State the blood parasite species.
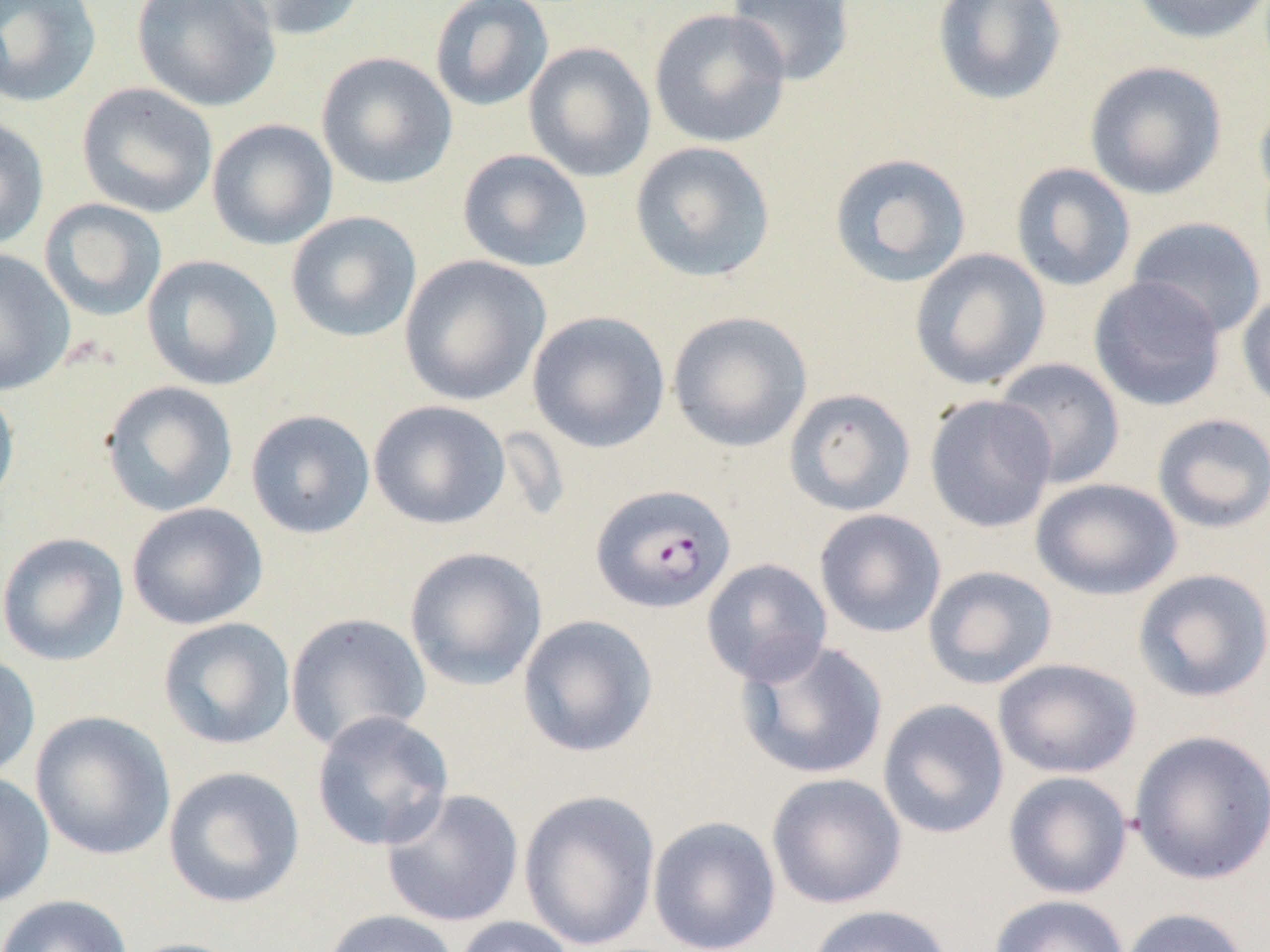

Plasmodium falciparum.

Approximate bounding boxes as (x1, y1, x2, y2) in pixels. Plasmodium falciparum-infected red blood cell locations: (590, 482, 736, 614). Uninfected red blood cell locations: (0, 0, 103, 108), (130, 0, 281, 112), (221, 0, 367, 41), (429, 0, 554, 112), (724, 0, 856, 86), (931, 0, 1068, 107), (1132, 0, 1270, 44), (648, 7, 792, 149), (523, 41, 657, 183), (316, 51, 458, 190), (1084, 61, 1227, 200), (76, 81, 219, 218), (1254, 91, 1270, 212), (0, 116, 50, 251), (206, 118, 338, 251), (629, 141, 777, 283), (456, 149, 593, 273), (827, 152, 972, 288), (1010, 162, 1136, 292), (39, 198, 167, 322), (285, 211, 422, 343), (1127, 216, 1267, 339), (0, 248, 76, 396), (909, 248, 1051, 391), (141, 254, 283, 391), (398, 255, 551, 406), (1088, 275, 1227, 411), (1236, 288, 1270, 414), (667, 310, 813, 453), (527, 311, 671, 453), (992, 358, 1126, 490), (100, 380, 238, 517), (0, 384, 20, 513), (783, 387, 917, 516), (924, 393, 1057, 533), (368, 399, 511, 530), (245, 409, 376, 539), (1151, 413, 1270, 534), (1030, 478, 1182, 601), (126, 502, 268, 630), (814, 509, 946, 638), (0, 531, 130, 666), (404, 546, 547, 691), (701, 558, 833, 687), (922, 565, 1058, 690), (1132, 568, 1270, 703), (285, 613, 432, 751), (517, 614, 659, 758), (157, 616, 296, 751), (734, 637, 889, 780), (0, 652, 41, 781), (994, 658, 1141, 779), (877, 699, 1010, 839), (30, 710, 176, 861), (311, 710, 455, 852), (1128, 728, 1270, 885), (162, 765, 305, 909), (1003, 771, 1133, 899), (766, 772, 907, 909), (0, 773, 55, 908), (380, 787, 525, 928), (518, 789, 661, 951), (647, 816, 782, 952), (0, 894, 134, 952), (988, 894, 1130, 952), (805, 904, 955, 952), (1118, 907, 1253, 952), (320, 909, 460, 952), (450, 916, 580, 952), (121, 937, 252, 952). Single field of view. Thin blood film. Light microscopy. Captured at 1000x magnification. Image is 1270×952 pixels.